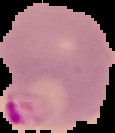
Result: malaria parasites identified. From a thin blood smear. Image is 115×133 pixels. The area outside the segmented cell region is set to black.